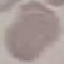
Summary:
  - Result: no malaria parasites detected
  - Image type: automatically extracted cell patch, resized to 64 × 64 pixels
  - Capture: smartphone camera at the microscope eyepiece
  - Stain: Giemsa
  - Preparation: thin blood smear